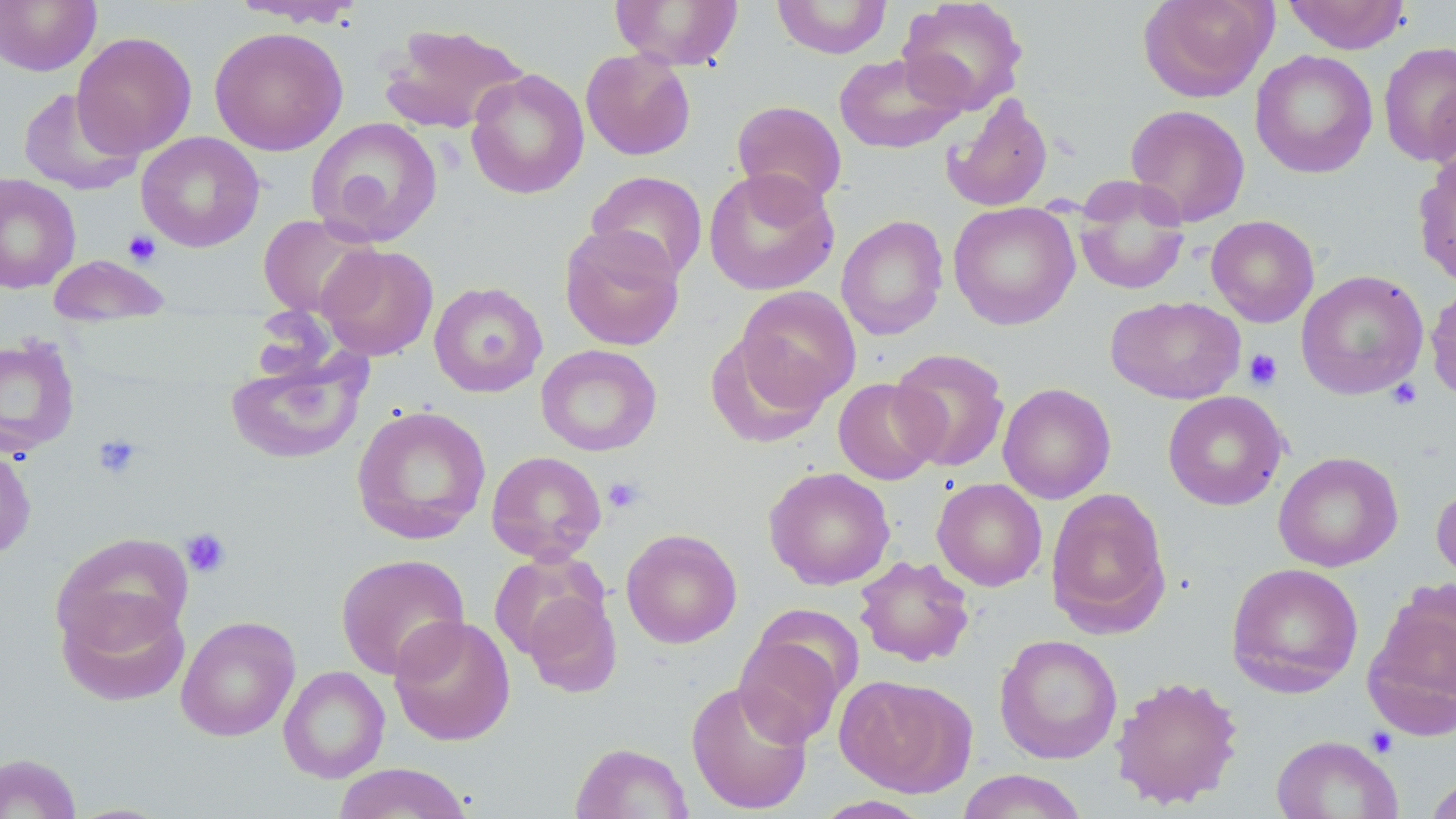

Approximate bounding boxes as (x1,y1)-(x2,y2) corner pairs in pixels. Uninfected red blood cell locations: (227,0)-(366,25), (610,0)-(744,69), (772,0)-(892,58), (897,0)-(1029,115), (1137,0)-(1277,103), (1282,0)-(1410,54), (0,1)-(101,76), (378,22)-(529,134), (209,26)-(348,156), (72,31)-(197,159), (1378,40)-(1456,167), (580,48)-(696,161), (1250,50)-(1378,179), (833,52)-(965,154), (465,68)-(589,200), (17,86)-(143,196), (943,92)-(1053,212), (731,100)-(847,209), (1125,103)-(1251,226), (306,117)-(443,246), (136,131)-(266,252), (1413,148)-(1456,289), (703,167)-(839,296), (585,170)-(709,283), (0,173)-(81,294), (1072,182)-(1191,296), (948,201)-(1080,330), (258,214)-(380,320), (836,215)-(949,341), (1206,215)-(1319,327), (559,225)-(685,351), (318,244)-(439,361), (48,254)-(171,327), (1295,270)-(1429,400), (429,281)-(547,397), (1425,281)-(1456,403), (734,286)-(861,409), (1105,295)-(1246,405), (706,333)-(829,447), (0,335)-(81,459), (536,344)-(662,457), (889,348)-(1011,472), (225,350)-(366,465), (833,377)-(943,485), (998,382)-(1116,504), (1162,391)-(1288,511), (351,405)-(491,545), (0,443)-(37,563), (486,450)-(606,564), (1273,451)-(1403,572), (762,466)-(896,590), (932,478)-(1047,591), (1431,480)-(1456,594), (1045,487)-(1171,635), (621,527)-(742,649), (51,533)-(194,657), (488,551)-(611,662), (335,552)-(470,680), (854,554)-(975,667), (1226,562)-(1364,698), (1365,581)-(1456,734), (520,588)-(622,697), (56,592)-(192,707), (175,615)-(300,742), (389,615)-(516,746), (732,625)-(853,748), (994,634)-(1123,764), (278,666)-(390,783), (835,674)-(977,797), (1110,674)-(1244,809), (686,679)-(813,815), (1271,735)-(1403,819), (571,742)-(693,819), (0,752)-(83,818), (332,762)-(473,819), (956,769)-(1089,819), (1423,772)-(1456,819), (812,795)-(934,818). Platelet locations: (122,230)-(162,267), (1243,349)-(1283,390), (1386,379)-(1422,410), (92,433)-(144,480), (604,477)-(645,513), (181,528)-(231,579), (1365,727)-(1398,758). Slide-level diagnosis: negative for blood parasites. Image is 1456×819 pixels. Single field of view. May-Grünwald-Giemsa-stained preparation. Thin blood film. 1000x magnification. Optical microscopy.